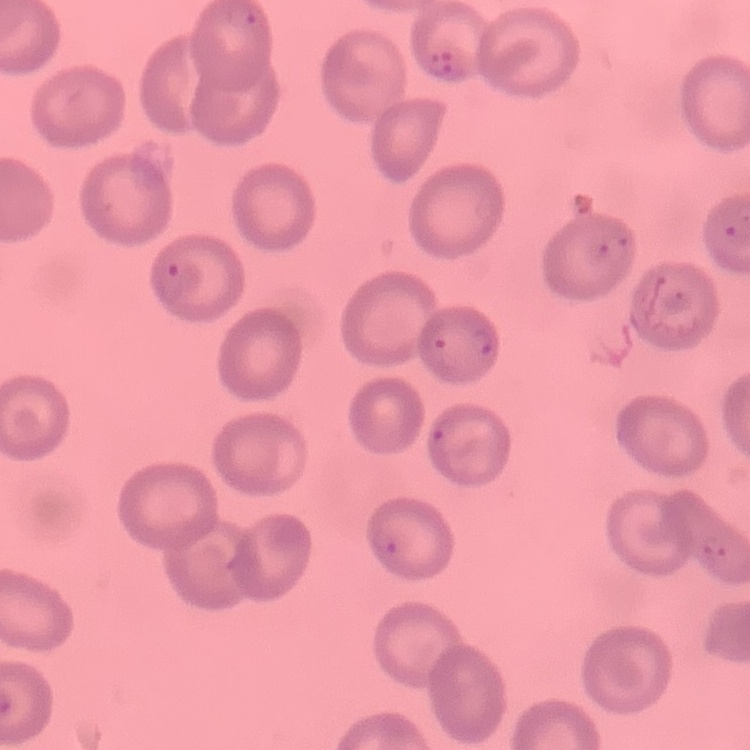

erythrocyte morphology = no rouleaux formation
stain = Field's or Giemsa
image type = one tile cut from a larger photomicrograph
preparation = thin blood smear